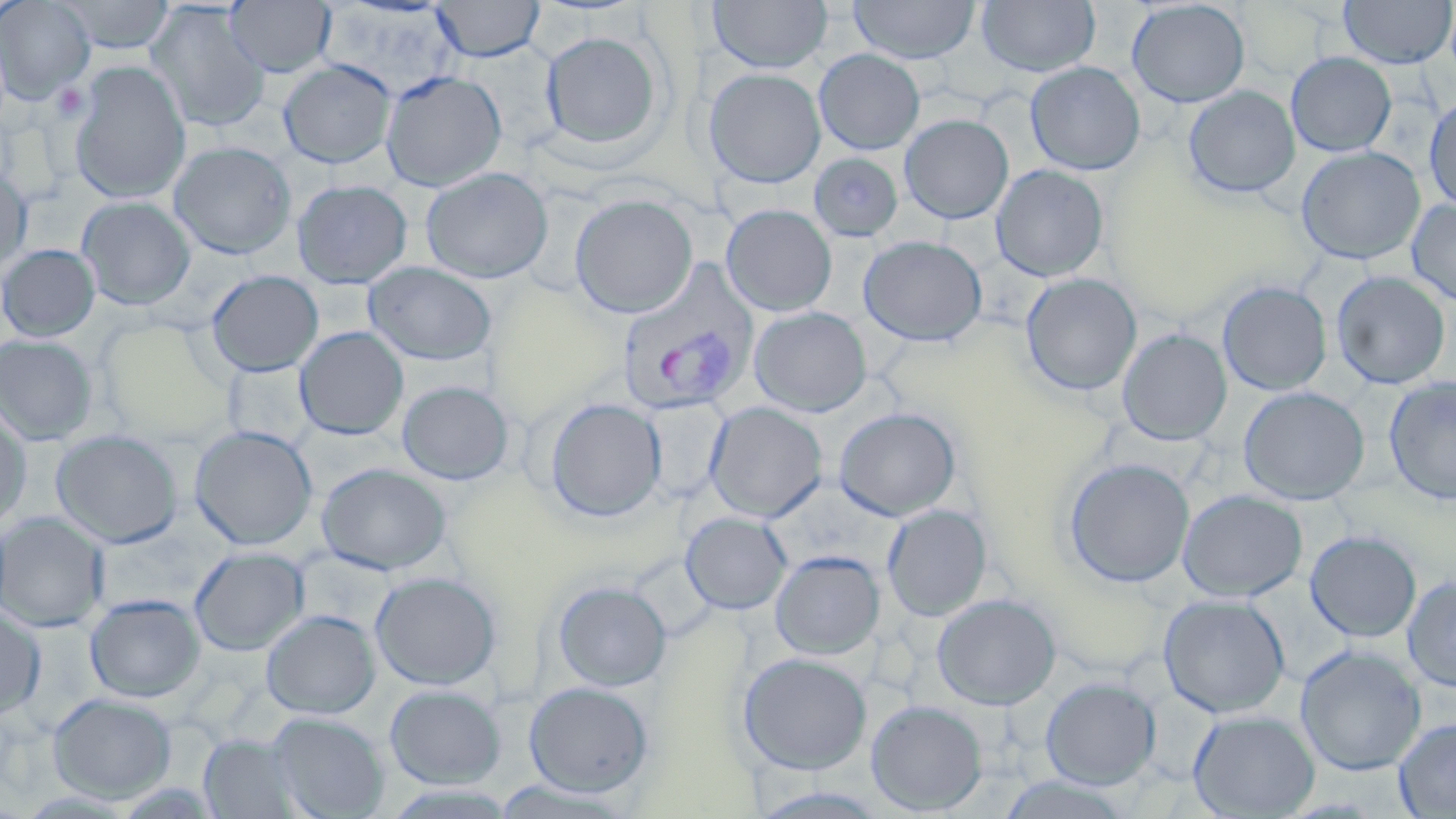

Summary:
  - Coordinate format: approximate bounding boxes as (x1, y1, x2, y2) in pixels
  - Uninfected red blood cell locations: (0, 0, 95, 104), (57, 0, 176, 54), (226, 0, 336, 78), (431, 0, 545, 61), (708, 0, 832, 74), (978, 0, 1099, 77), (1126, 0, 1250, 108), (1339, 0, 1455, 69), (849, 1, 979, 64), (146, 2, 270, 132), (320, 5, 462, 101), (540, 30, 665, 151), (814, 49, 925, 155), (1286, 52, 1396, 157), (279, 59, 396, 168), (70, 61, 191, 203), (1025, 61, 1145, 176), (704, 68, 826, 189), (381, 70, 506, 191), (1183, 85, 1300, 199), (1424, 93, 1456, 212), (900, 114, 1014, 224), (169, 141, 296, 259), (1295, 146, 1426, 265), (809, 152, 904, 241), (991, 164, 1109, 281), (0, 166, 32, 276), (421, 167, 553, 284), (292, 180, 413, 289), (570, 193, 698, 319), (77, 197, 195, 310), (1406, 199, 1456, 307), (721, 204, 837, 316), (858, 235, 987, 347), (0, 244, 100, 342), (364, 261, 497, 366), (206, 270, 324, 377), (1331, 271, 1451, 390), (1020, 273, 1142, 396), (1217, 281, 1332, 396), (749, 307, 872, 417), (295, 326, 409, 440), (1117, 329, 1232, 445), (0, 335, 98, 446), (1384, 376, 1456, 506), (397, 380, 514, 485), (1238, 387, 1370, 505), (543, 397, 667, 522), (639, 398, 729, 503), (704, 402, 827, 522), (0, 407, 32, 531), (834, 407, 961, 520), (190, 425, 317, 550), (51, 430, 182, 548), (1063, 457, 1195, 587), (317, 462, 451, 575), (1178, 489, 1308, 601), (882, 504, 992, 620), (681, 512, 792, 614), (0, 513, 109, 633), (1305, 530, 1422, 642), (190, 547, 309, 656), (770, 551, 884, 659), (370, 571, 501, 690), (1402, 575, 1456, 692), (552, 580, 672, 691), (85, 594, 205, 703), (932, 594, 1061, 709), (1157, 594, 1290, 718), (0, 606, 46, 720), (261, 610, 380, 719), (1295, 644, 1426, 776), (737, 652, 872, 774), (1040, 676, 1161, 789), (524, 681, 654, 797), (384, 684, 506, 789), (48, 693, 177, 802), (866, 700, 987, 815), (1188, 709, 1320, 818), (266, 712, 388, 819), (1393, 716, 1456, 818), (200, 733, 306, 818), (993, 774, 1135, 818)
  - Platelet locations: (52, 82, 89, 122)
  - Plasmodium vivax-infected red blood cell locations: (616, 260, 759, 416)
  - Slide-level diagnosis: Plasmodium vivax
  - Stain: May-Grünwald-Giemsa
  - Magnification: 1000x
  - Field of view: one of a larger specimen
  - Modality: optical microscopy
  - Preparation: thin blood smear
  - Image size: 1456×819 pixels